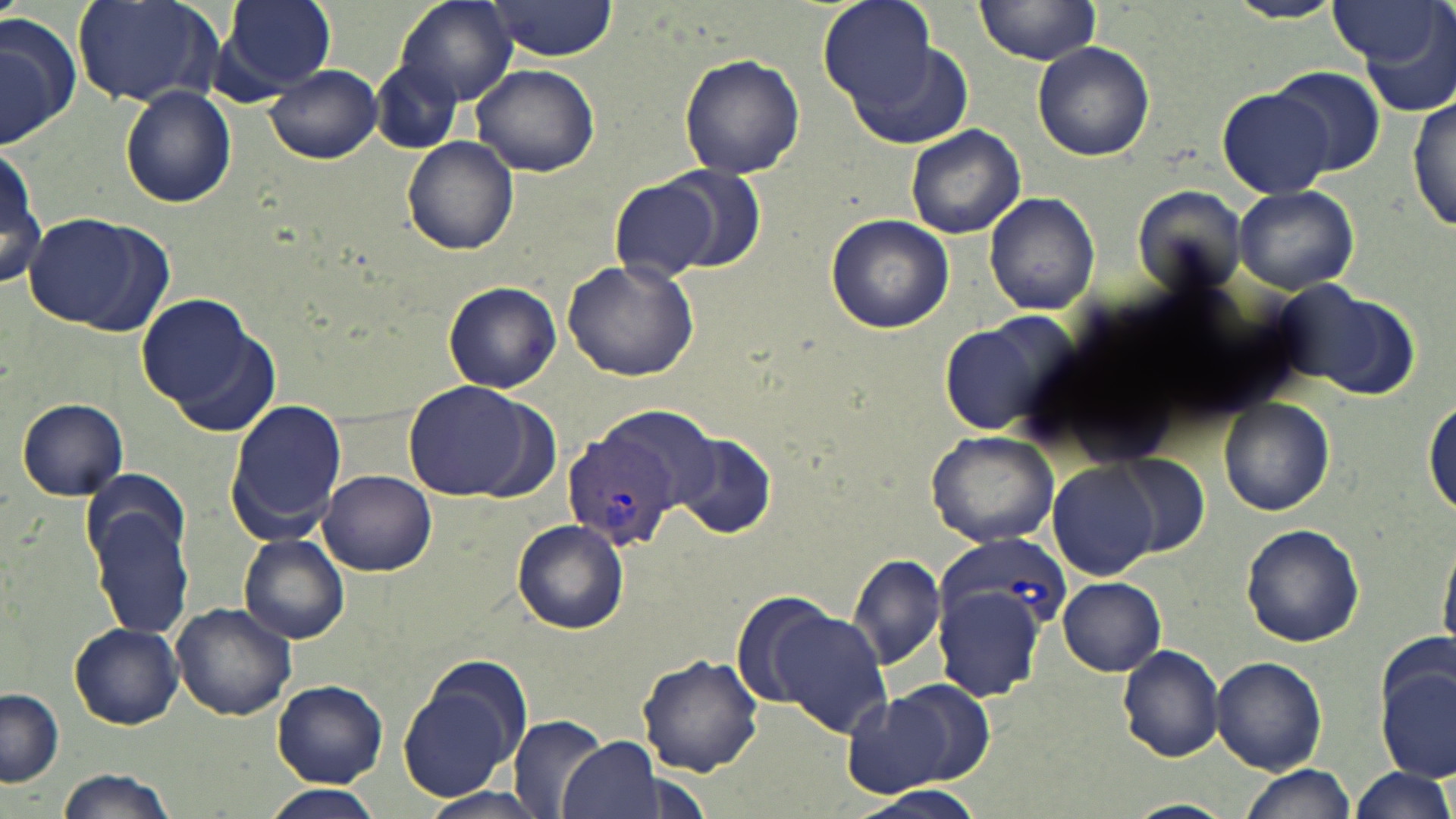

Approximate bounding boxes as named x1/y1/x2/y2 corners in pixels. Uninfected red blood cell locations: (x1=72, y1=0, x2=228, y2=109), (x1=221, y1=0, x2=337, y2=94), (x1=395, y1=0, x2=519, y2=107), (x1=816, y1=0, x2=937, y2=112), (x1=975, y1=0, x2=1103, y2=64), (x1=483, y1=1, x2=624, y2=62), (x1=1225, y1=1, x2=1346, y2=25), (x1=1328, y1=3, x2=1448, y2=68), (x1=0, y1=12, x2=79, y2=148), (x1=1362, y1=14, x2=1456, y2=117), (x1=843, y1=39, x2=976, y2=148), (x1=1032, y1=41, x2=1155, y2=162), (x1=677, y1=54, x2=805, y2=179), (x1=372, y1=59, x2=462, y2=153), (x1=471, y1=64, x2=599, y2=176), (x1=266, y1=65, x2=381, y2=165), (x1=1264, y1=69, x2=1385, y2=177), (x1=119, y1=86, x2=235, y2=207), (x1=1214, y1=86, x2=1337, y2=200), (x1=1410, y1=93, x2=1455, y2=235), (x1=906, y1=125, x2=1027, y2=241), (x1=404, y1=138, x2=518, y2=255), (x1=0, y1=143, x2=44, y2=289), (x1=652, y1=169, x2=765, y2=272), (x1=609, y1=177, x2=721, y2=283), (x1=1136, y1=184, x2=1252, y2=295), (x1=1233, y1=184, x2=1360, y2=293), (x1=984, y1=191, x2=1099, y2=316), (x1=27, y1=212, x2=161, y2=331), (x1=823, y1=212, x2=954, y2=333), (x1=562, y1=258, x2=700, y2=383), (x1=443, y1=281, x2=561, y2=393), (x1=1293, y1=289, x2=1420, y2=399), (x1=138, y1=293, x2=268, y2=418), (x1=938, y1=312, x2=1077, y2=439), (x1=403, y1=380, x2=543, y2=500), (x1=226, y1=397, x2=348, y2=542), (x1=1219, y1=397, x2=1335, y2=516), (x1=16, y1=398, x2=130, y2=500), (x1=1423, y1=399, x2=1455, y2=517), (x1=597, y1=403, x2=725, y2=511), (x1=924, y1=429, x2=1061, y2=548), (x1=673, y1=433, x2=777, y2=539), (x1=1109, y1=455, x2=1211, y2=556), (x1=1047, y1=463, x2=1160, y2=580), (x1=319, y1=471, x2=437, y2=575), (x1=84, y1=484, x2=195, y2=646), (x1=512, y1=519, x2=628, y2=635), (x1=1240, y1=523, x2=1366, y2=647), (x1=238, y1=534, x2=350, y2=644), (x1=1433, y1=538, x2=1456, y2=661), (x1=847, y1=552, x2=947, y2=670), (x1=1058, y1=578, x2=1166, y2=676), (x1=934, y1=579, x2=1049, y2=702), (x1=729, y1=594, x2=839, y2=711), (x1=170, y1=603, x2=297, y2=720), (x1=770, y1=608, x2=893, y2=739), (x1=68, y1=622, x2=183, y2=729), (x1=1379, y1=628, x2=1453, y2=719), (x1=1117, y1=644, x2=1225, y2=763), (x1=638, y1=652, x2=765, y2=777), (x1=1210, y1=655, x2=1326, y2=774), (x1=395, y1=662, x2=531, y2=801), (x1=1378, y1=665, x2=1456, y2=781), (x1=874, y1=679, x2=996, y2=788), (x1=271, y1=680, x2=388, y2=787), (x1=0, y1=688, x2=63, y2=788), (x1=838, y1=689, x2=953, y2=798), (x1=508, y1=714, x2=609, y2=819), (x1=558, y1=737, x2=662, y2=819), (x1=57, y1=766, x2=182, y2=819), (x1=1239, y1=766, x2=1353, y2=819), (x1=1349, y1=767, x2=1455, y2=819), (x1=844, y1=784, x2=987, y2=819), (x1=264, y1=786, x2=379, y2=819), (x1=418, y1=788, x2=552, y2=819), (x1=1122, y1=798, x2=1234, y2=819). Plasmodium vivax-infected red blood cell locations: (x1=561, y1=430, x2=677, y2=549), (x1=937, y1=533, x2=1071, y2=643). Slide-level diagnosis: Plasmodium vivax. May-Grünwald-Giemsa stain. Thin blood smear. Image is 1456×819 pixels. Single field of view. Captured at 1000x magnification. Light microscopy.